Locate and identify every blood parasite.
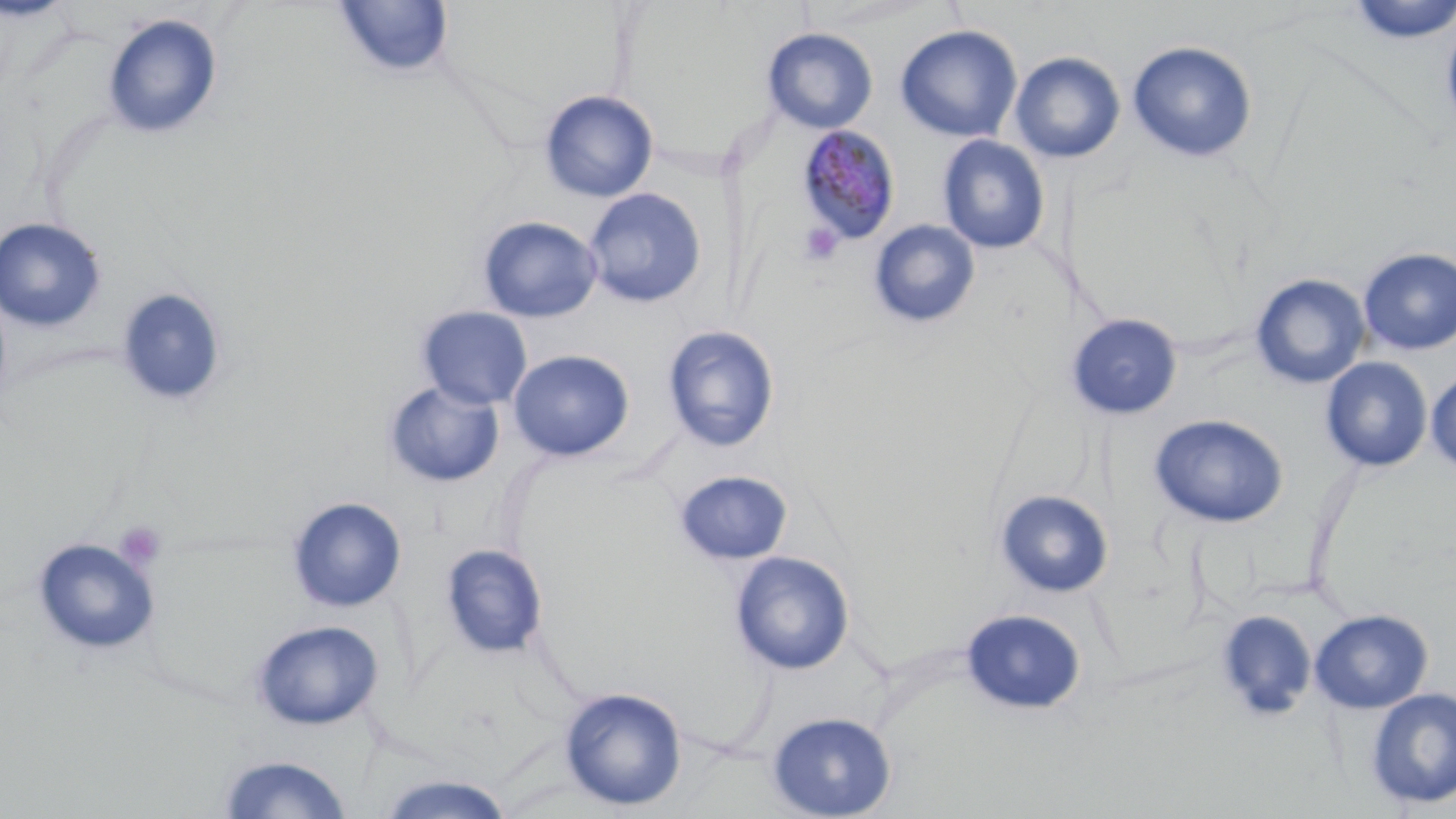

Approximate bounding boxes as named x1/y1/x2/y2 corners in pixels.
Plasmodium malariae-infected red blood cells: (x1=797, y1=126, x2=901, y2=246).
No Plasmodium falciparum, Plasmodium ovale, Plasmodium vivax, Babesia divergens, or Trypanosoma brucei observed.

slide_level_diagnosis: Plasmodium malariae
platelet_locations: 'approximate bounding boxes as named x1/y1/x2/y2 corners in pixels: (x1=798, y1=222, x2=845, y2=266), (x1=114, y1=520, x2=168, y2=572)'
modality: optical microscopy
stain: May-Grünwald-Giemsa
uninfected_red_blood_cell_locations: 'approximate bounding boxes as named x1/y1/x2/y2 corners in pixels: (x1=1345, y1=0, x2=1456, y2=45), (x1=332, y1=2, x2=454, y2=79), (x1=102, y1=13, x2=223, y2=140), (x1=1440, y1=16, x2=1456, y2=141), (x1=895, y1=24, x2=1023, y2=142), (x1=761, y1=27, x2=878, y2=133), (x1=1127, y1=41, x2=1258, y2=163), (x1=1010, y1=51, x2=1125, y2=163), (x1=539, y1=89, x2=659, y2=203), (x1=936, y1=135, x2=1050, y2=254), (x1=584, y1=188, x2=707, y2=308), (x1=478, y1=216, x2=602, y2=324), (x1=0, y1=217, x2=106, y2=333), (x1=868, y1=219, x2=981, y2=328), (x1=1358, y1=247, x2=1456, y2=355), (x1=1250, y1=273, x2=1370, y2=389), (x1=116, y1=287, x2=227, y2=407), (x1=417, y1=306, x2=533, y2=410), (x1=1066, y1=313, x2=1183, y2=420), (x1=662, y1=325, x2=780, y2=453), (x1=507, y1=349, x2=634, y2=462), (x1=1320, y1=356, x2=1433, y2=472), (x1=1426, y1=372, x2=1456, y2=474), (x1=384, y1=380, x2=505, y2=488), (x1=1149, y1=414, x2=1288, y2=527), (x1=674, y1=470, x2=793, y2=566), (x1=993, y1=489, x2=1114, y2=599), (x1=287, y1=497, x2=407, y2=612), (x1=32, y1=537, x2=160, y2=656), (x1=439, y1=543, x2=548, y2=660), (x1=730, y1=551, x2=855, y2=675), (x1=960, y1=608, x2=1086, y2=716), (x1=1310, y1=608, x2=1433, y2=714), (x1=1214, y1=610, x2=1317, y2=723), (x1=252, y1=619, x2=383, y2=729), (x1=559, y1=686, x2=688, y2=811), (x1=1365, y1=687, x2=1456, y2=810), (x1=766, y1=711, x2=897, y2=819), (x1=214, y1=753, x2=356, y2=818), (x1=371, y1=773, x2=519, y2=818)'
field_of_view: one of a larger specimen
image_size: 1456×819 pixels
preparation: thin blood smear
magnification: 1000x